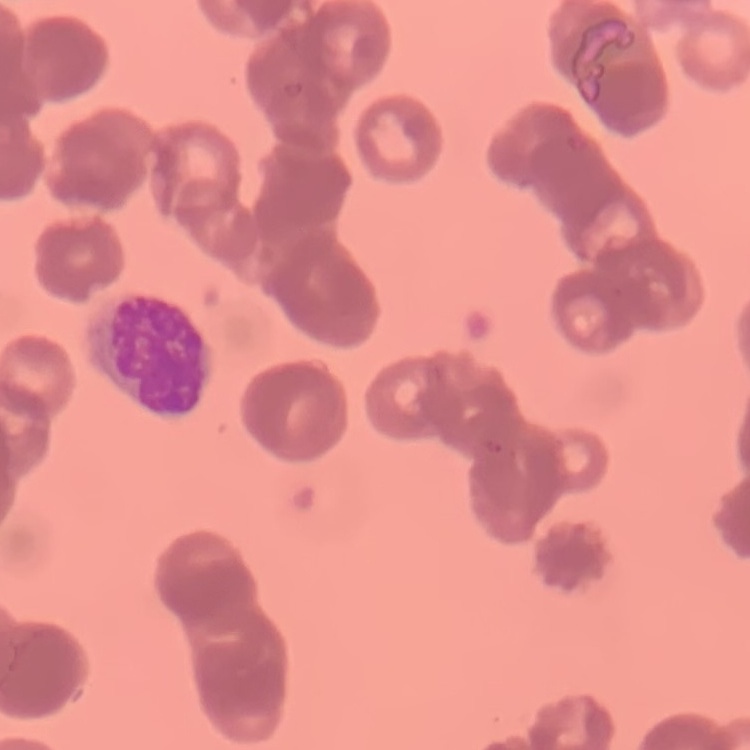 The erythrocytes exhibit rouleaux formation. Thin peripheral smear. Field's or Giemsa stain. One tile cut from a larger photomicrograph.